Locate every Plasmodium ovale-infected red blood cell.
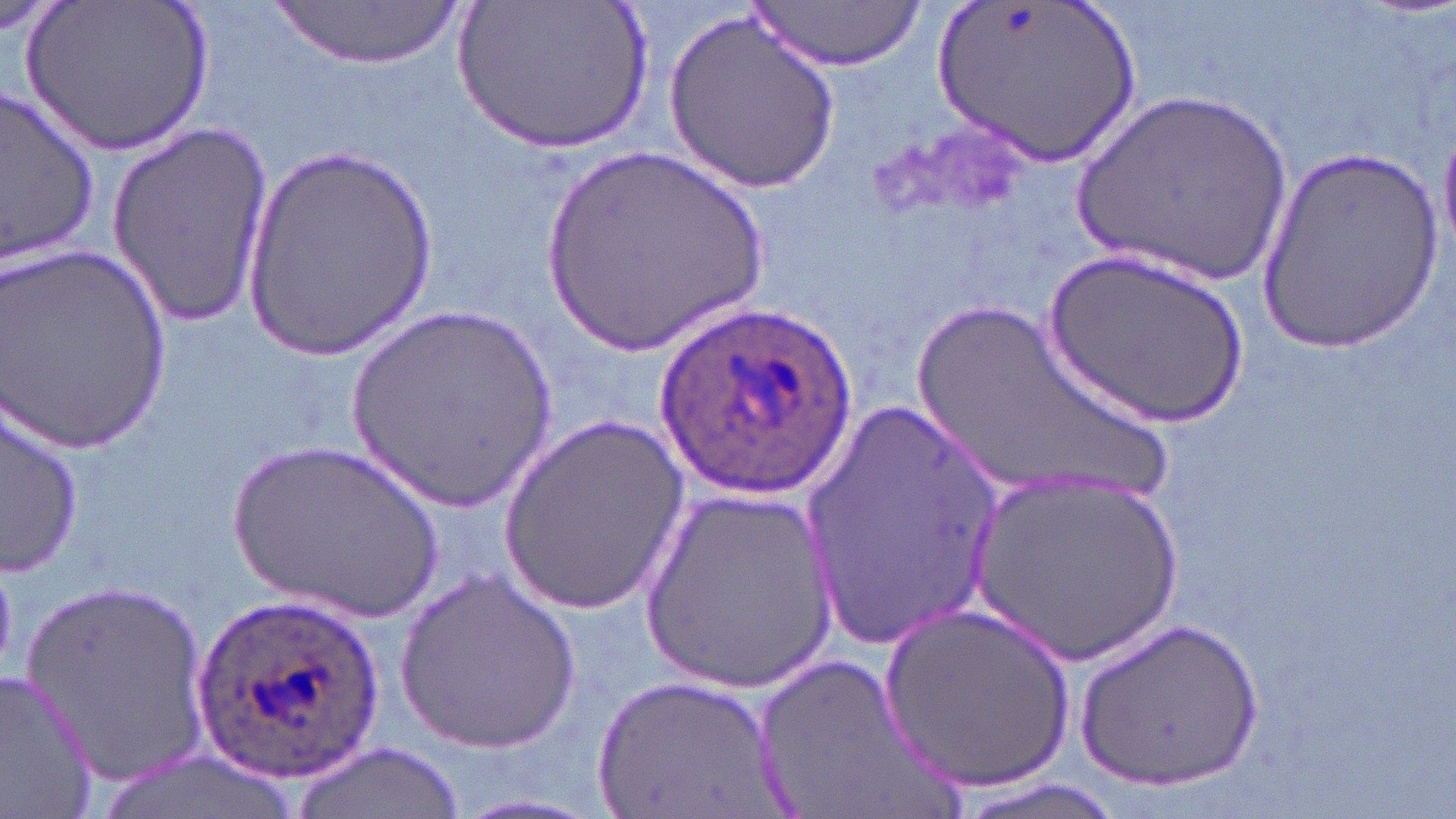

Approximate bounding boxes as (x1, y1, x2, y2) in pixels.
Plasmodium ovale-infected red blood cells: (659, 312, 855, 488), (192, 589, 387, 779).

Summary:
  - Uninfected red blood cell locations: (25, 0, 216, 159), (455, 0, 657, 157), (935, 0, 1140, 166), (268, 1, 464, 69), (748, 1, 925, 72), (663, 9, 841, 194), (0, 88, 103, 264), (1069, 89, 1300, 287), (1439, 113, 1456, 259), (104, 122, 273, 322), (241, 142, 443, 359), (534, 143, 778, 364), (1249, 143, 1447, 355), (1, 245, 169, 454), (1043, 250, 1249, 430), (908, 298, 1174, 511), (342, 306, 561, 514), (798, 398, 1013, 646), (3, 402, 83, 581), (497, 412, 690, 609), (228, 438, 449, 628), (970, 470, 1186, 664), (637, 484, 841, 693), (395, 568, 582, 751), (22, 577, 218, 787), (875, 600, 1077, 795), (1077, 615, 1264, 793), (747, 650, 955, 819), (0, 669, 104, 818), (592, 672, 783, 819), (291, 741, 457, 817)
  - Slide-level diagnosis: Plasmodium ovale
  - Preparation: thin blood film
  - Field of view: one of a larger specimen
  - Magnification: 1000x
  - Image size: 1456×819 pixels
  - Stain: May-Grünwald-Giemsa
  - Modality: optical microscopy